Identify the cell.
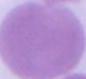
This is an erythrocyte.

Micrograph. 1000x magnification.